Give the preparation type.
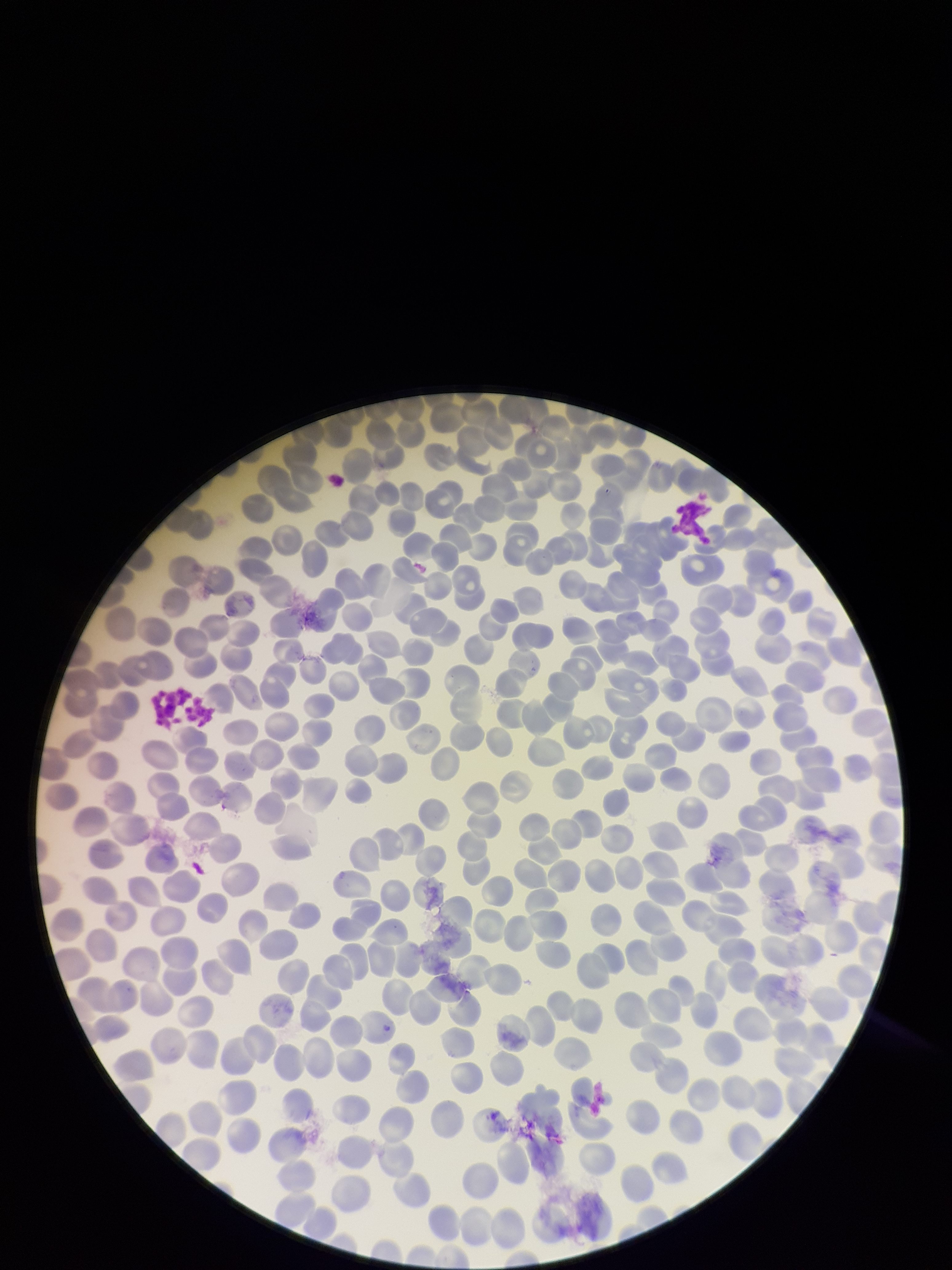

Thin.

patient malaria status = negative
image size = 952×1270 pixels
parasitized red blood cell count = 0
capture = smartphone photograph through the microscope eyepiece
red blood cell count = 220
parasitized red blood cells = none identified
stain = Giemsa
field of view = one from this slide